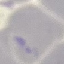 Result: no malaria parasites detected. Giemsa-stained preparation. Photographed with a smartphone camera at the microscope eyepiece. Thin blood smear. Cell patch, automatically extracted from a larger field of view and resized to 64 × 64 pixels.